State the blood parasite species.
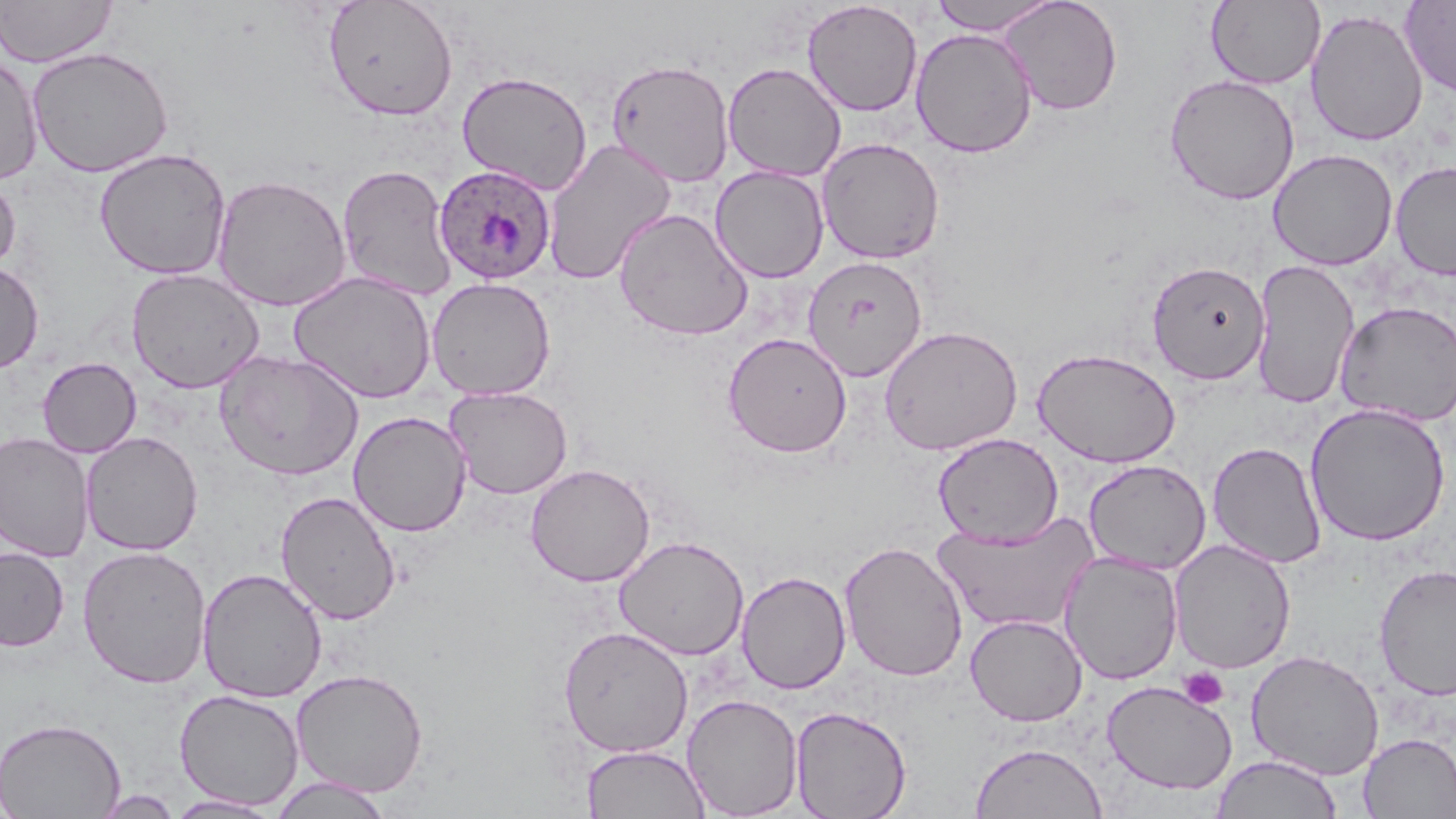
Plasmodium ovale.

uninfected red blood cell locations = approximate bounding boxes as (x1,y1)-(x2,y2) corner pairs in pixels: (0,0)-(118,67), (322,0)-(459,121), (928,0)-(1062,35), (998,0)-(1123,116), (1400,0)-(1456,98), (802,1)-(923,117), (1206,1)-(1325,89), (1305,8)-(1429,147), (910,28)-(1037,158), (26,46)-(175,178), (0,54)-(44,186), (606,58)-(735,187), (722,62)-(846,182), (457,71)-(593,195), (1164,74)-(1300,205), (543,138)-(677,286), (817,138)-(945,264), (94,148)-(231,280), (1267,149)-(1398,270), (1390,160)-(1456,281), (337,163)-(458,301), (710,165)-(830,283), (0,172)-(21,277), (211,174)-(352,312), (614,208)-(753,341), (802,255)-(928,382), (1250,259)-(1360,409), (1146,260)-(1270,385), (0,261)-(44,374), (126,268)-(264,393), (289,271)-(437,403), (427,277)-(556,400), (1334,301)-(1456,426), (878,324)-(1023,455), (722,332)-(852,457), (1032,347)-(1181,467), (215,349)-(364,481), (37,357)-(141,458), (444,386)-(573,499), (1305,403)-(1451,547), (348,411)-(472,537), (80,431)-(203,556), (0,432)-(95,562), (932,433)-(1063,546), (1207,440)-(1327,569), (1083,459)-(1211,575), (525,463)-(655,586), (275,490)-(402,625), (934,511)-(1099,634), (614,535)-(749,660), (1169,539)-(1296,674), (839,540)-(968,682), (77,545)-(213,688), (0,546)-(69,652), (1060,552)-(1183,684), (1374,563)-(1456,702), (197,568)-(328,703), (737,570)-(851,694), (965,614)-(1088,727), (557,624)-(693,758), (1246,649)-(1385,781), (290,668)-(429,797), (1102,680)-(1237,795), (174,688)-(304,810), (681,693)-(803,818), (790,705)-(911,819), (0,717)-(126,819), (1358,732)-(1456,818), (969,742)-(1108,819), (582,745)-(710,819), (1211,753)-(1342,819), (268,776)-(395,818), (92,790)-(183,818), (164,794)-(283,817)
Plasmodium ovale-infected red blood cell locations = approximate bounding boxes as (x1,y1)-(x2,y2) corner pairs in pixels: (433,164)-(557,285)
magnification = 1000x
stain = May-Grünwald-Giemsa
modality = light microscopy
image size = 1456×819 pixels
field of view = single
platelet locations = approximate bounding boxes as (x1,y1)-(x2,y2) corner pairs in pixels: (1179,667)-(1229,710)
preparation = thin blood film